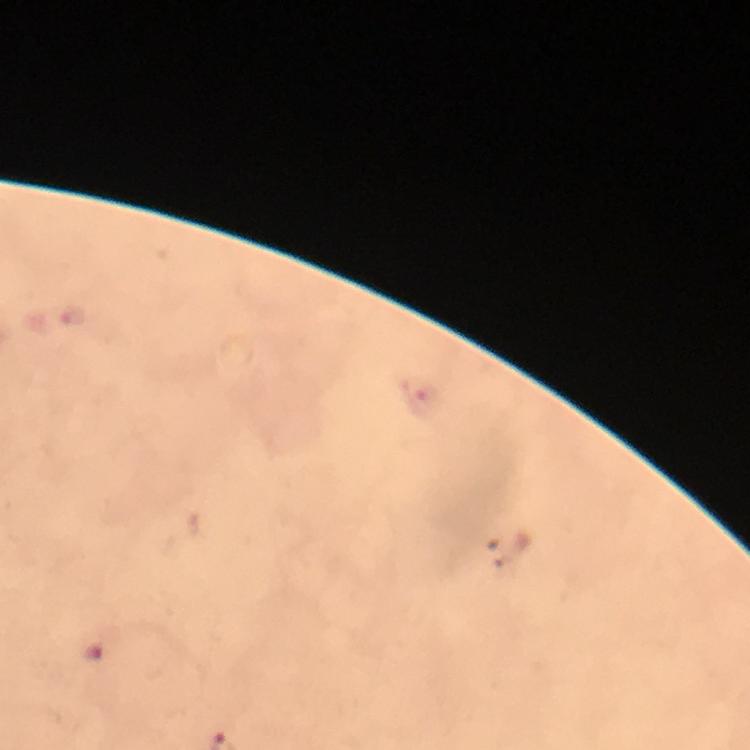

context = from a malaria diagnostic workup
preparation = thick smear
malaria parasite locations = approximate centers as (x, y) in pixels: (74, 316), (96, 648)
cropped from = one field of view
magnification = 100x
stain = Giemsa
image size = 750×750 pixels
capture = smartphone mounted on the microscope
immersion oil = applied